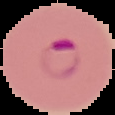
image size = 115×115 pixels
malaria status = parasitized
image type = cell region segmented out of the field of view; surrounding area masked to black
preparation = thin blood film